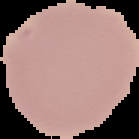

malaria status = uninfected
image size = 139×139 pixels
image type = segmented cell region with the area outside set to black
preparation = thin blood film